State which cell type is depicted.
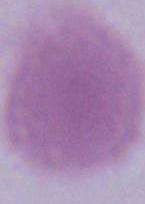
An erythrocyte.

magnification = 1000x
modality = micrograph